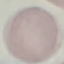

malaria_status: uninfected
image_type: cell patch, automatically extracted from a larger field of view and resized to 64 × 64 pixels
preparation: thin blood film
capture: smartphone camera at the microscope eyepiece
stain: Giemsa